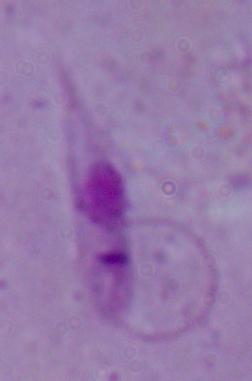 1000x magnification. A Leishmania parasite is shown. Micrograph.